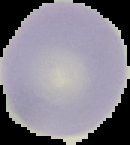

image size = 130×145 pixels
image type = segmented cell region with the area outside set to black
preparation = thin blood film
result = no Plasmodium parasites detected